Assess this cell for malaria.
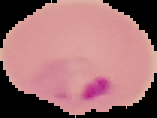
It is parasitized.

image size = 157×118 pixels
image type = segmented cell region with the area outside set to black
preparation = thin blood film